State which cell type is depicted.
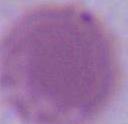
This is an erythrocyte.

Summary:
  - Modality: photomicrograph
  - Magnification: 1000x